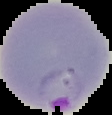

preparation = thin blood film
image size = 112×115 pixels
image type = segmented cell region on a black background
result = malaria parasites identified